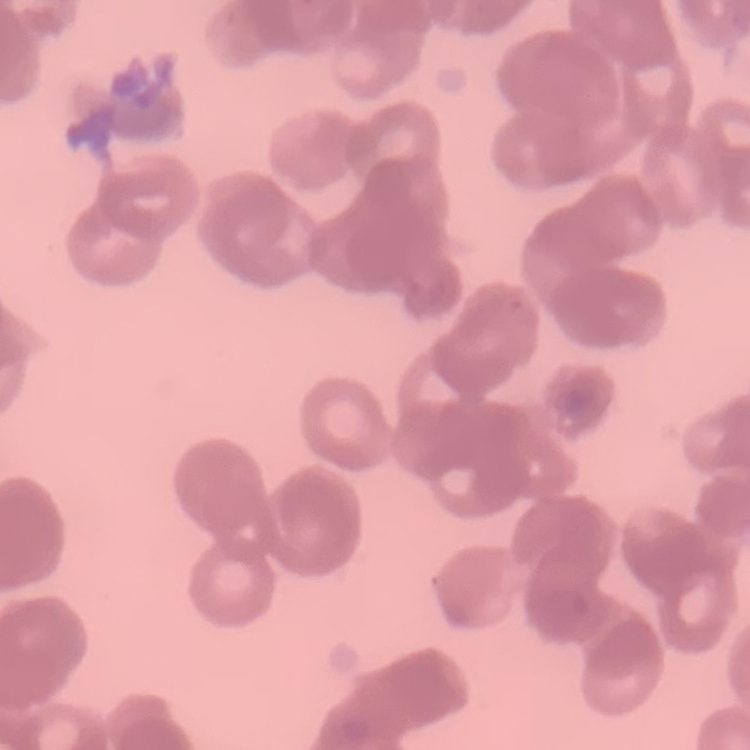
The red blood cells exhibit rouleaux formation. Square crop of a larger photomicrograph. Field's or Giemsa stain. Thin blood film.